State the preparation type.
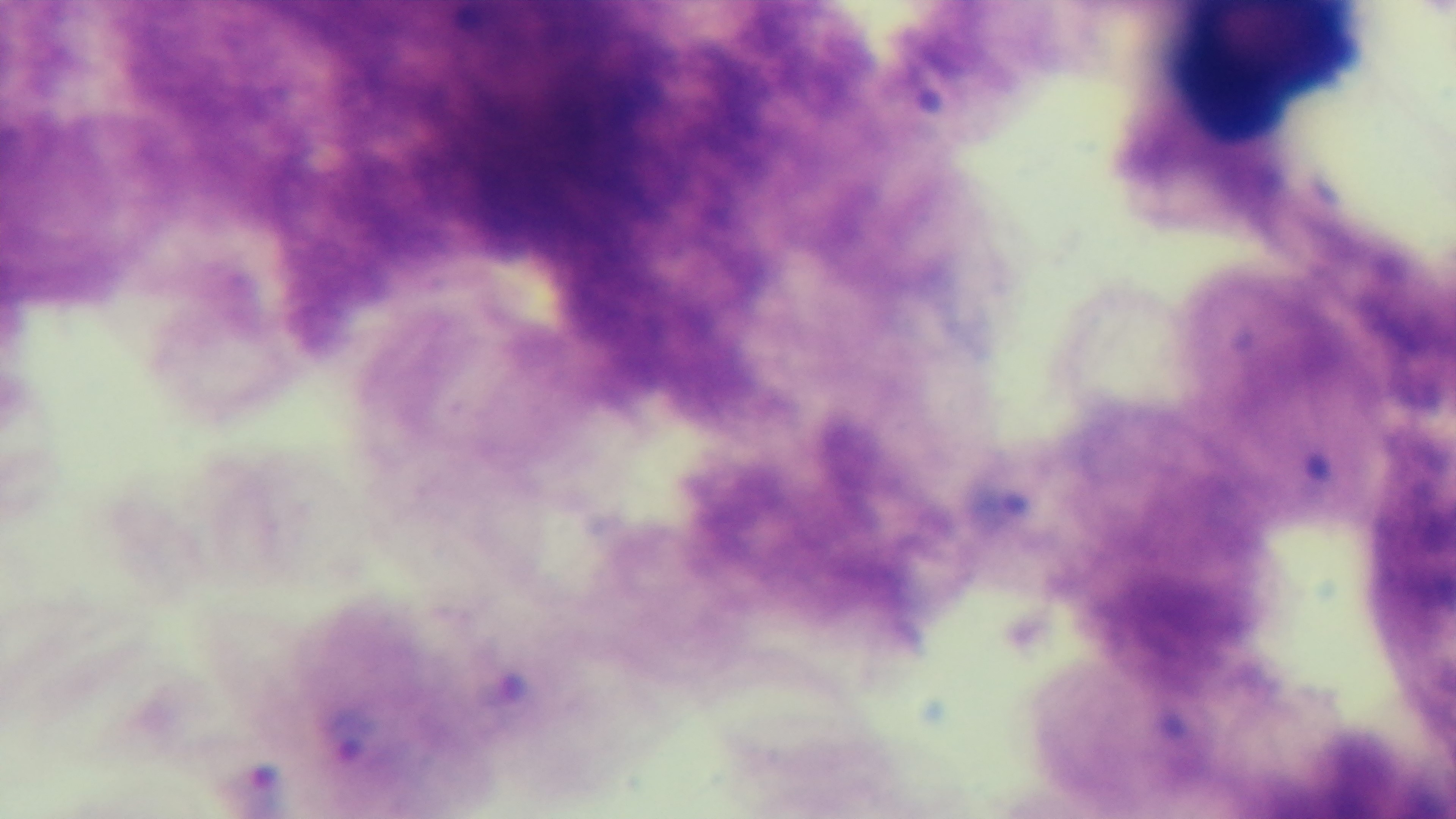

Thick.

Captured with a mounted 4K digital camera. One field from the slide. Light microscopy. Malaria status: infected. Giemsa-stained. Oil-immersion objective, 100x.